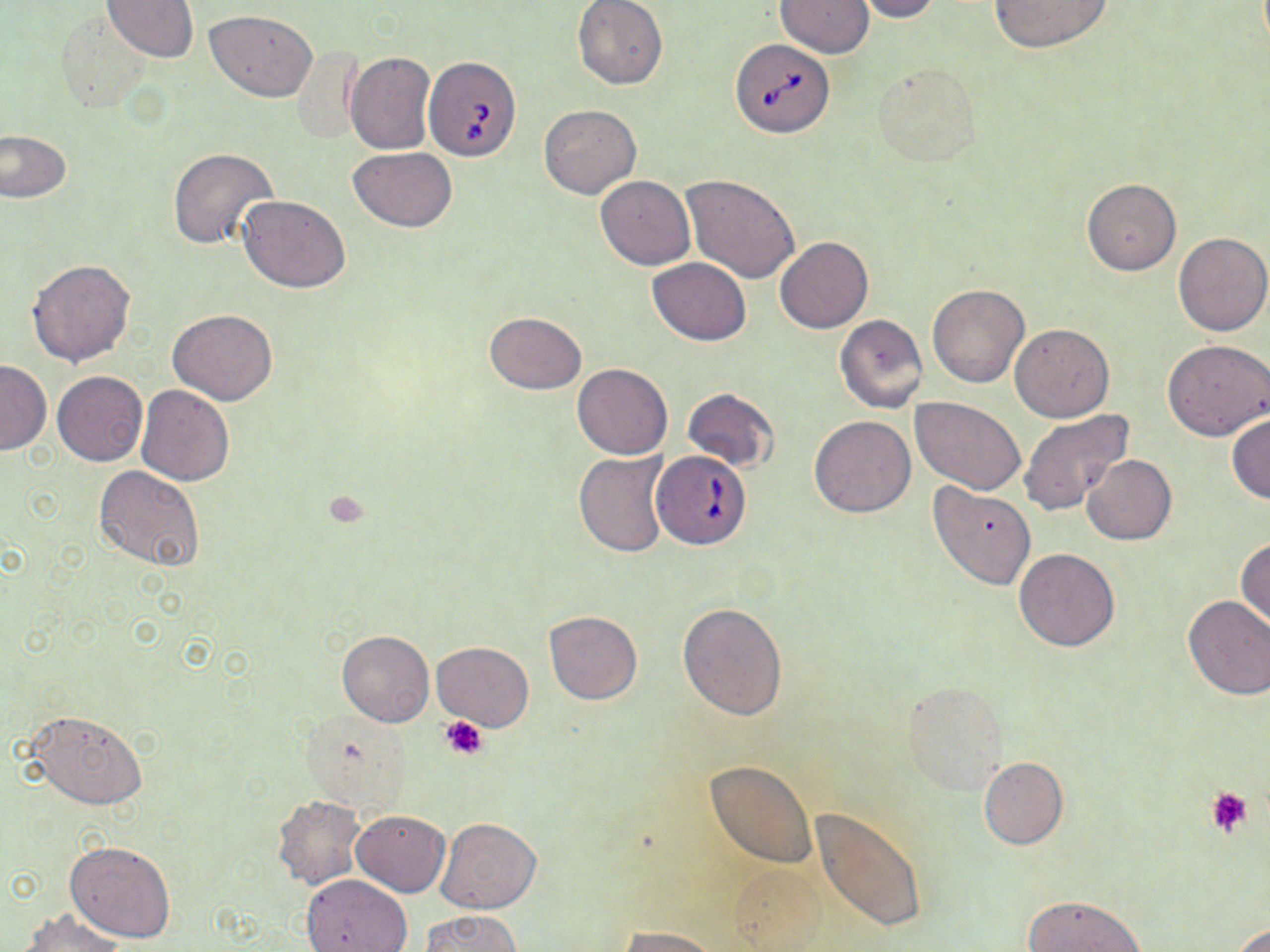
Approximate bounding boxes as named x1/y1/x2/y2 corners in pixels. Babesia divergens-infected red blood cell locations: (x1=731, y1=38, x2=833, y2=138), (x1=423, y1=54, x2=522, y2=163), (x1=651, y1=449, x2=753, y2=549). Platelet locations: (x1=441, y1=715, x2=488, y2=759), (x1=1206, y1=787, x2=1253, y2=838). Uninfected red blood cell locations: (x1=104, y1=0, x2=197, y2=61), (x1=572, y1=0, x2=668, y2=89), (x1=853, y1=0, x2=941, y2=22), (x1=987, y1=0, x2=1113, y2=52), (x1=774, y1=1, x2=874, y2=56), (x1=206, y1=9, x2=317, y2=100), (x1=54, y1=10, x2=152, y2=112), (x1=293, y1=45, x2=363, y2=146), (x1=346, y1=51, x2=436, y2=154), (x1=873, y1=63, x2=980, y2=166), (x1=539, y1=104, x2=642, y2=199), (x1=0, y1=129, x2=71, y2=202), (x1=167, y1=147, x2=279, y2=252), (x1=348, y1=147, x2=456, y2=230), (x1=683, y1=174, x2=799, y2=283), (x1=594, y1=175, x2=695, y2=270), (x1=1082, y1=178, x2=1180, y2=275), (x1=238, y1=195, x2=351, y2=292), (x1=1173, y1=232, x2=1270, y2=336), (x1=774, y1=236, x2=872, y2=333), (x1=648, y1=257, x2=750, y2=344), (x1=26, y1=259, x2=137, y2=366), (x1=928, y1=284, x2=1030, y2=387), (x1=168, y1=309, x2=279, y2=405), (x1=483, y1=311, x2=587, y2=394), (x1=834, y1=314, x2=929, y2=413), (x1=1011, y1=323, x2=1113, y2=421), (x1=1161, y1=338, x2=1270, y2=440), (x1=0, y1=360, x2=51, y2=454), (x1=572, y1=364, x2=672, y2=459), (x1=52, y1=370, x2=148, y2=466), (x1=137, y1=384, x2=234, y2=485), (x1=682, y1=387, x2=779, y2=472), (x1=911, y1=396, x2=1024, y2=493), (x1=1020, y1=409, x2=1135, y2=515), (x1=1227, y1=414, x2=1270, y2=503), (x1=809, y1=415, x2=916, y2=517), (x1=574, y1=451, x2=669, y2=557), (x1=1083, y1=454, x2=1177, y2=545), (x1=93, y1=465, x2=205, y2=571), (x1=928, y1=483, x2=1035, y2=590), (x1=1236, y1=537, x2=1270, y2=633), (x1=1013, y1=548, x2=1119, y2=651), (x1=1181, y1=595, x2=1270, y2=700), (x1=677, y1=602, x2=787, y2=721), (x1=543, y1=610, x2=643, y2=705), (x1=337, y1=630, x2=434, y2=727), (x1=432, y1=642, x2=534, y2=731), (x1=902, y1=683, x2=1007, y2=794), (x1=26, y1=707, x2=149, y2=810), (x1=300, y1=711, x2=414, y2=811), (x1=977, y1=756, x2=1067, y2=850), (x1=703, y1=761, x2=818, y2=870), (x1=272, y1=795, x2=365, y2=889), (x1=814, y1=806, x2=929, y2=936), (x1=352, y1=809, x2=449, y2=896), (x1=436, y1=816, x2=540, y2=913), (x1=65, y1=841, x2=176, y2=944), (x1=725, y1=863, x2=831, y2=949), (x1=301, y1=873, x2=412, y2=952), (x1=1023, y1=894, x2=1146, y2=951), (x1=20, y1=909, x2=127, y2=952), (x1=420, y1=911, x2=524, y2=952), (x1=1231, y1=922, x2=1270, y2=951), (x1=616, y1=926, x2=720, y2=951). Slide-level diagnosis: Babesia divergens. Image is 1270×952 pixels. Thin blood film. Captured at 1000x magnification. Optical microscopy. May-Grünwald-Giemsa stain. One field of a larger specimen.